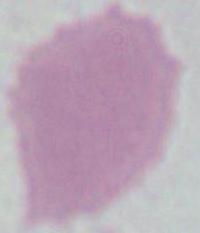
identification = red blood cell
magnification = 1000x
modality = photomicrograph